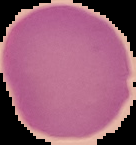
Summary:
  - Malaria status: uninfected
  - Image type: cell region segmented out of the field of view; surrounding area masked to black
  - Image size: 136×145 pixels
  - Preparation: thin blood film